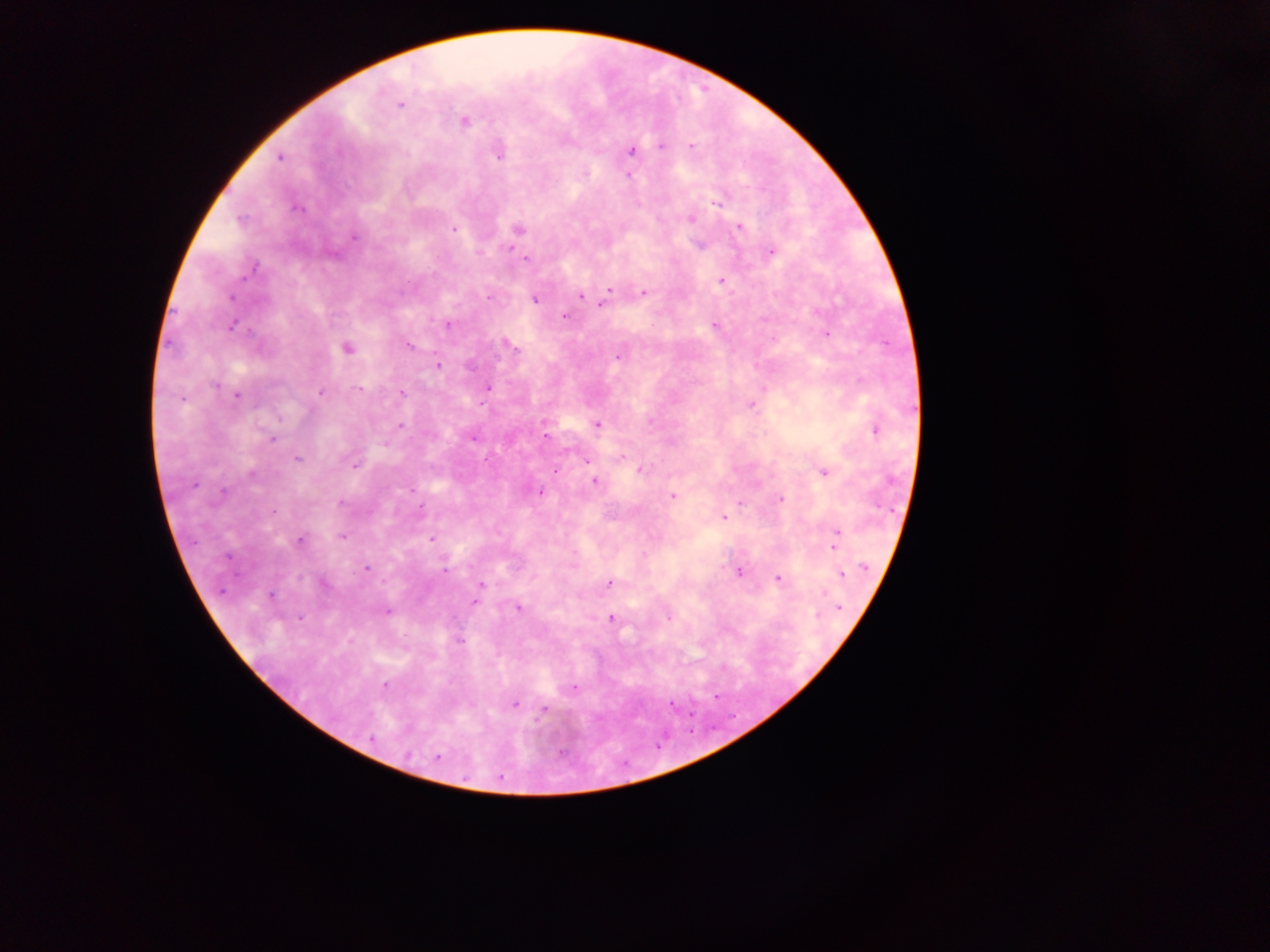
Approximate centers as (x, y) in pixels. Malaria parasite locations: (400, 104), (465, 121), (691, 145), (662, 146), (632, 151), (499, 157), (280, 158), (628, 175), (717, 203), (297, 208), (691, 218), (240, 220), (739, 228), (518, 229), (454, 230), (354, 236), (510, 249), (770, 252), (526, 259), (251, 271), (722, 281), (609, 290), (643, 292), (579, 296), (488, 297), (232, 298), (536, 300), (602, 304), (564, 316), (448, 324), (715, 325), (231, 327), (826, 335), (408, 345), (514, 348), (347, 349), (618, 357), (438, 366), (215, 384), (488, 388), (359, 389), (320, 393), (402, 394), (236, 396), (752, 405), (400, 425), (597, 425), (876, 431), (545, 436), (474, 438), (272, 439), (297, 459), (587, 461), (354, 466), (640, 469), (555, 470), (823, 472), (252, 475), (593, 481), (193, 485), (410, 490), (540, 492), (222, 493), (672, 496), (780, 499), (340, 502), (740, 502), (421, 508), (273, 512), (723, 517), (836, 531), (342, 537), (431, 539), (836, 539), (300, 541), (227, 556), (865, 567), (366, 569), (444, 570), (739, 572), (843, 574), (778, 579), (609, 583), (482, 585), (478, 590), (824, 593), (271, 595), (475, 602), (840, 607), (518, 608), (387, 612), (817, 614), (299, 618), (610, 618), (668, 619), (405, 636), (461, 642), (385, 685), (572, 689), (514, 704), (671, 704), (543, 709), (371, 739), (407, 754), (438, 757). Image is 1270×952 pixels. Single field of view. Thick blood film. Collected in Ghana. Mobile-phone photograph taken through the microscope.